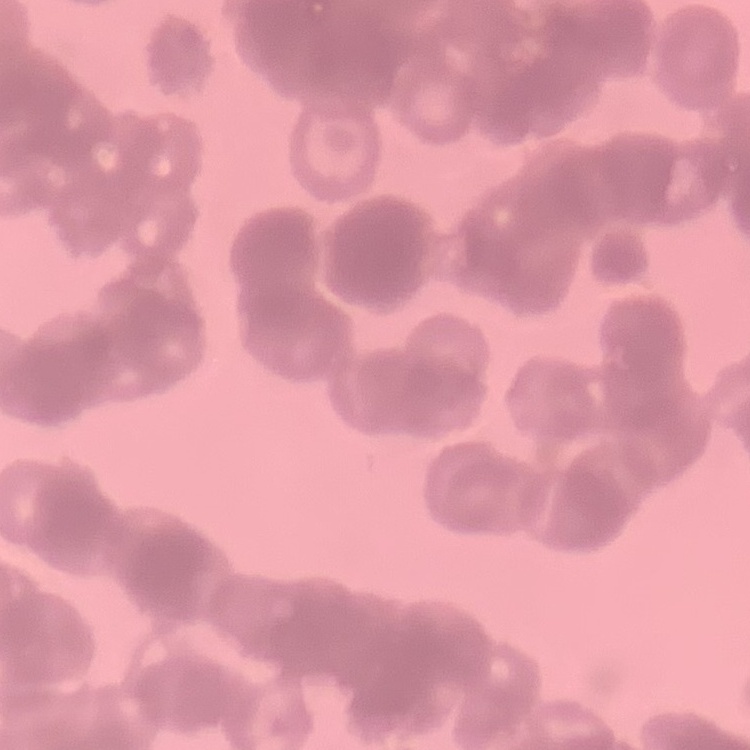
Summary:
  - Erythrocyte morphology: rouleaux formation
  - Stain: Field's or Giemsa
  - Image type: one tile cut from a larger photomicrograph
  - Preparation: thin blood smear